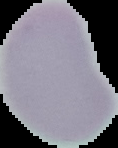
Summary:
  - Result: no Plasmodium parasites detected
  - Preparation: thin blood smear
  - Image size: 118×148 pixels
  - Image type: cell region segmented out of the field of view; surrounding area masked to black